Draw a bounding box around every parasitised red blood cell, every trophozoite, every gametocyte, every leukocyte, and every artifact (platelet-like body, stain precipitate, or debris).
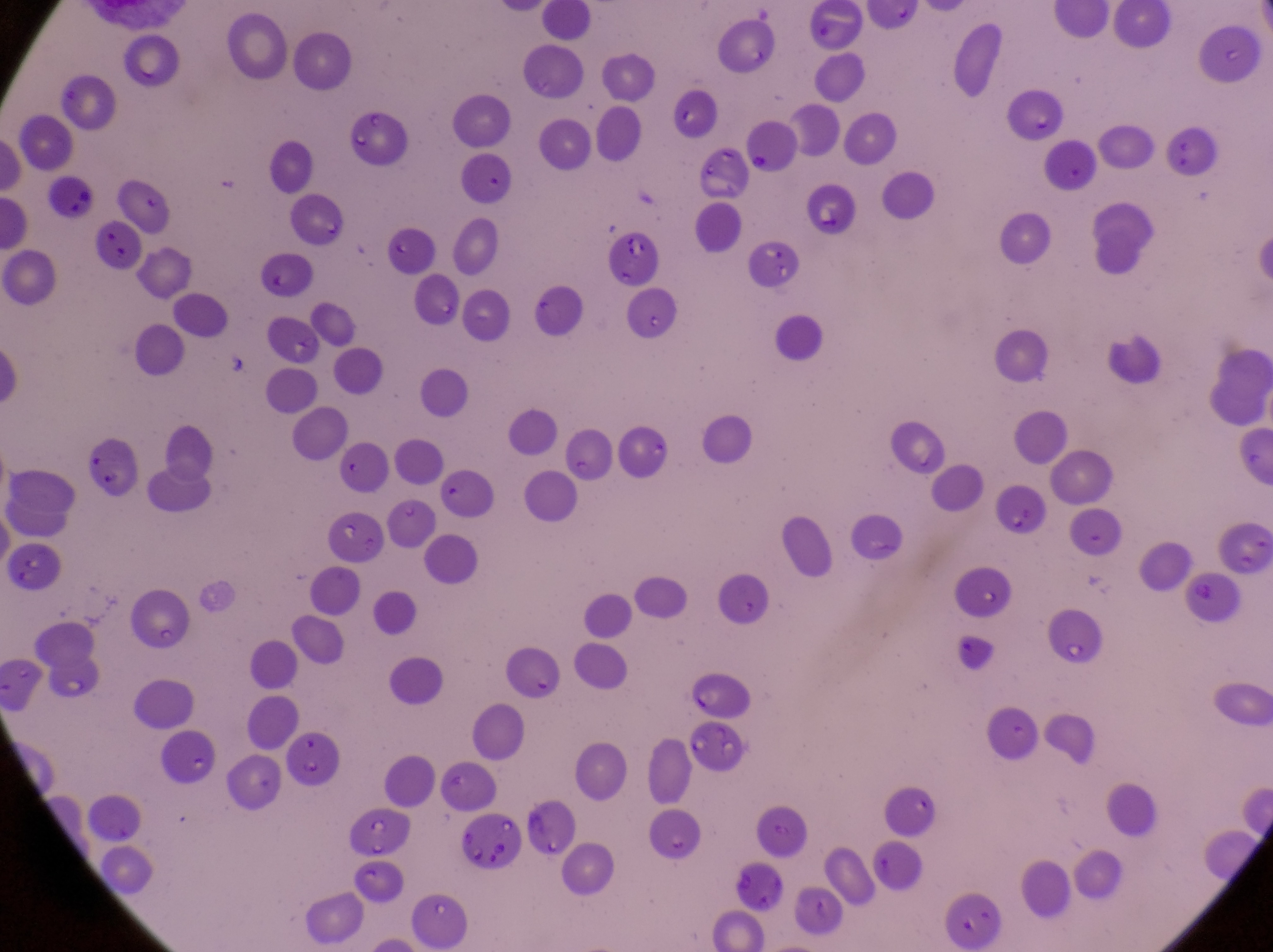
Approximate bounding boxes as (left, top, right, bottom) in pixels.
Parasitised red blood cells: (602, 229, 659, 292), (1181, 570, 1244, 628), (1046, 604, 1108, 669), (464, 807, 531, 875).
No leukocytes observed.
Artifacts (platelet-like body, stain precipitate, or debris): (893, 422, 948, 475).

Summary:
  - Image size: 1273×952 pixels
  - Country: Uganda
  - Preparation: thin blood film
  - Magnification: 1000x
  - Field of view: single
  - Capture: smartphone photograph through the eyepiece of an Olympus CX-23 microscope